Describe the morphology of the red blood cells.
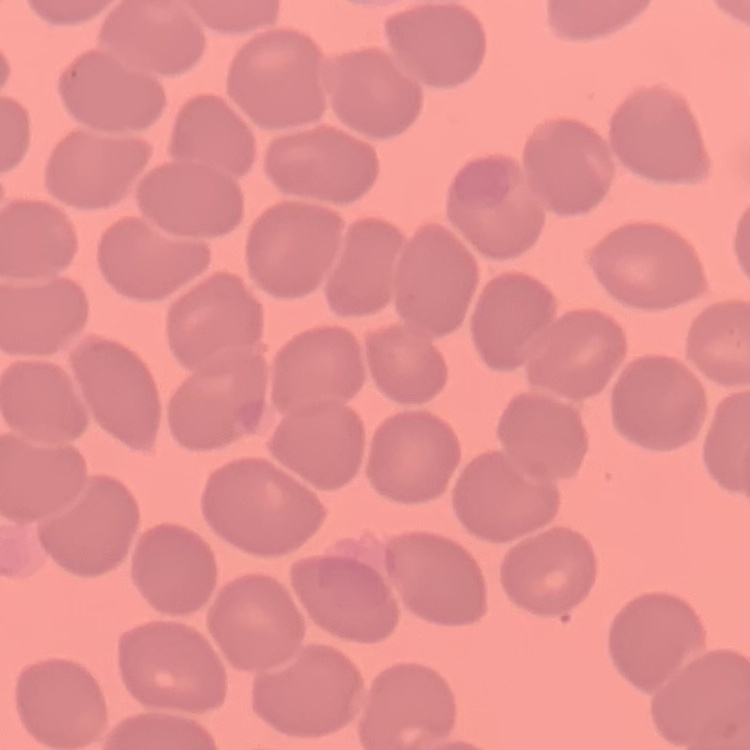

No rouleaux formation.

Thin peripheral smear. One tile cut from a larger photomicrograph. Field's or Giemsa stain.